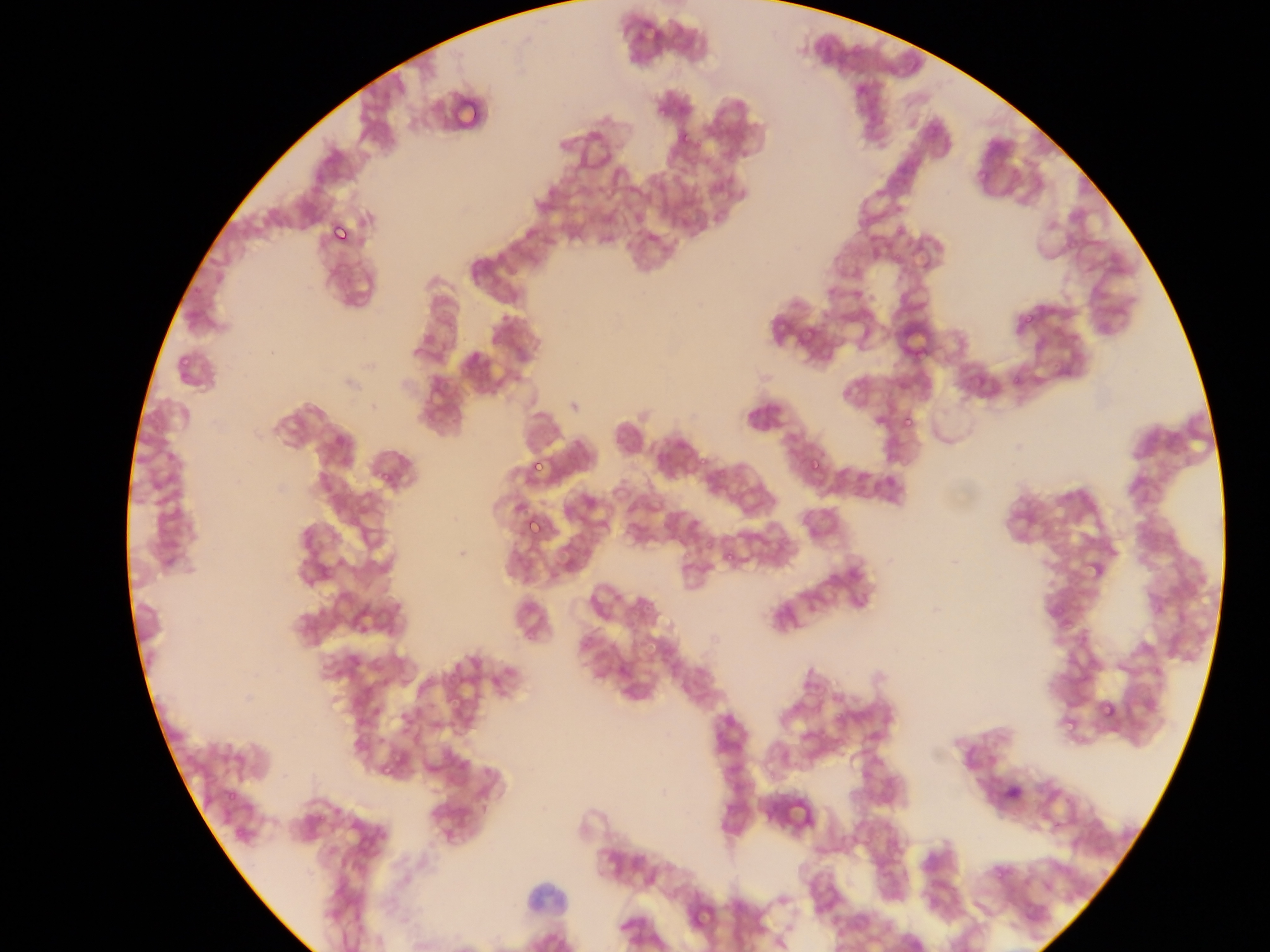

Approximate bounding boxes as [left, top, right, bottom] in pixels.
Summary:
  - Plasmodium parasite locations: [325, 215, 360, 252], [1021, 314, 1036, 330], [900, 412, 920, 434], [527, 455, 550, 479], [804, 457, 829, 469], [529, 518, 543, 536], [653, 642, 676, 668], [1099, 700, 1119, 721], [1061, 718, 1079, 731], [383, 762, 396, 780]
  - Field of view: single
  - Preparation: thin blood film
  - Country: Ghana
  - Capture: mobile-phone photograph through a microscope
  - Image size: 1270×952 pixels